State which parasite is depicted.
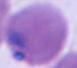

This is Plasmodium.

Captured at either 400x or 1000x magnification. Photomicrograph.